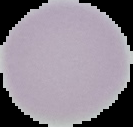 From a thin blood smear. Malaria status: uninfected. The area outside the segmented cell region is set to black. Image is 133×127 pixels.